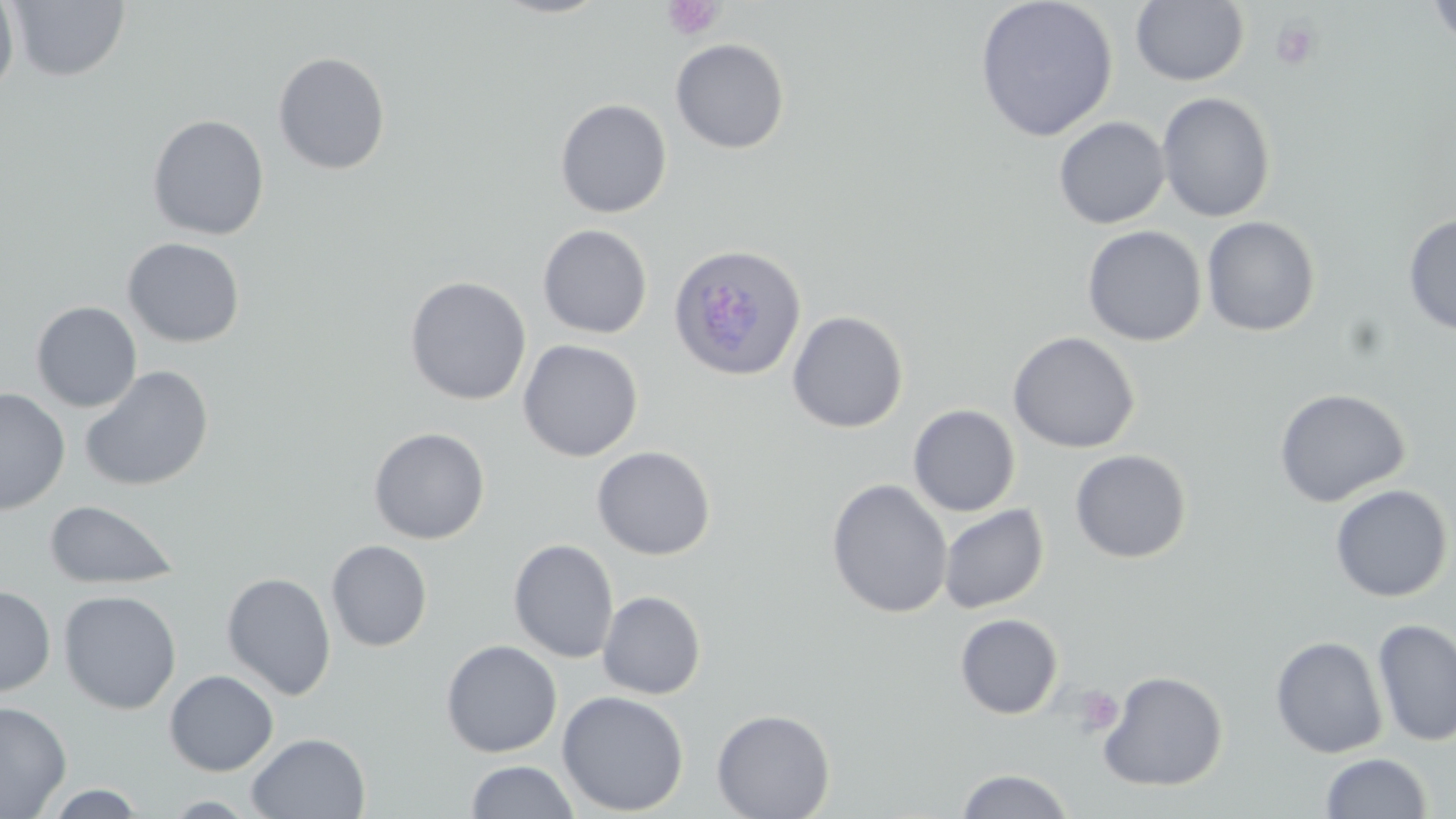
Approximate bounding boxes as [x1, y1, x2, y2] in pixels. Uninfected red blood cell locations: [491, 0, 611, 19], [974, 0, 1119, 142], [1425, 0, 1456, 49], [0, 1, 19, 99], [7, 1, 131, 82], [1130, 1, 1250, 87], [670, 38, 790, 154], [273, 51, 391, 175], [1157, 92, 1276, 223], [554, 98, 673, 218], [147, 114, 269, 240], [1054, 116, 1170, 229], [1062, 117, 1190, 326], [1402, 213, 1456, 336], [1201, 216, 1321, 337], [537, 224, 653, 339], [1082, 225, 1207, 347], [122, 237, 246, 348], [404, 276, 532, 405], [30, 301, 143, 412], [787, 310, 909, 433], [1008, 331, 1141, 453], [518, 339, 643, 462], [79, 365, 214, 492], [0, 388, 70, 515], [1274, 388, 1411, 507], [908, 404, 1021, 517], [368, 426, 490, 545], [592, 445, 716, 560], [1070, 449, 1192, 563], [827, 479, 953, 618], [1329, 483, 1454, 603], [44, 499, 180, 590], [939, 503, 1050, 614], [508, 539, 619, 663], [326, 540, 433, 652], [222, 572, 336, 700], [0, 586, 56, 696], [58, 589, 182, 714], [598, 590, 706, 699], [954, 613, 1064, 719], [1373, 618, 1456, 747], [1270, 634, 1388, 759], [441, 639, 562, 758], [1097, 669, 1229, 792], [164, 670, 279, 776], [556, 690, 689, 816], [0, 700, 72, 818], [711, 708, 836, 819], [246, 732, 371, 818], [1319, 751, 1433, 818], [463, 760, 580, 819], [955, 768, 1075, 819], [44, 784, 147, 818], [158, 795, 264, 817]. Plasmodium ovale-infected red blood cell locations: [668, 243, 808, 381]. Platelet locations: [662, 0, 725, 41], [1271, 19, 1319, 70], [1075, 686, 1124, 735]. Slide-level diagnosis: Plasmodium ovale. Captured at 1000x magnification. Optical microscopy. Single field of view. Image is 1456×819 pixels. May-Grünwald-Giemsa stain. Thin blood film.